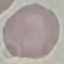
Malaria status: uninfected. Automatically extracted cell patch, resized to 64 × 64 pixels. Giemsa stain. Photographed with a smartphone camera at the microscope eyepiece. Thin smear of blood.